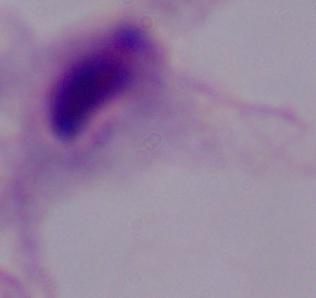 Captured at 1000x magnification. A trichomonad is seen. Photomicrograph.